Name the parasite shown.
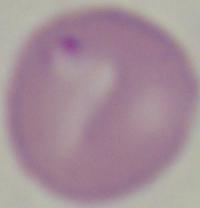
Babesia.

Summary:
  - Modality: photomicrograph
  - Magnification: 1000x